Locate Plasmodium parasites and leukocytes.
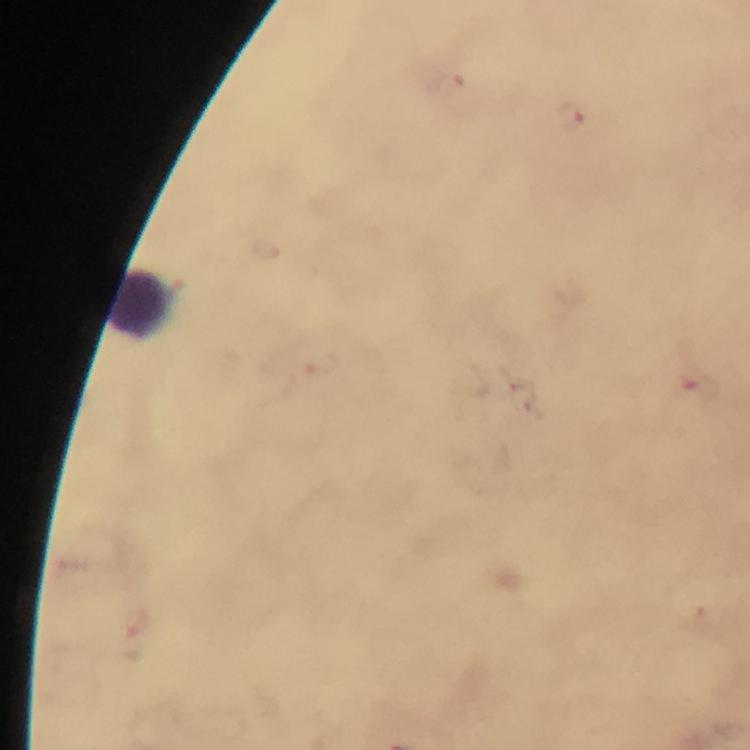
Approximate centers as (x, y) in pixels.
Plasmodium parasites: (570, 118).
Leukocytes: (144, 306).

From a diagnostic examination for malaria. A crop from one field of view. Thick blood smear. Photographed through the microscope with a smartphone camera. 100x magnification. Image is 750×750 pixels. Immersion oil was used. Giemsa-stained preparation.